Report the malaria status of this cell.
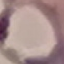
It is parasitized.

Summary:
  - Stain: Giemsa
  - Image type: automatically extracted cell patch, resized to 64 × 64 pixels
  - Preparation: thin blood smear
  - Capture: smartphone camera at the microscope eyepiece